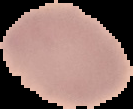
Summary:
  - Image type: segmented cell region on a black background
  - Preparation: thin blood film
  - Result: no malaria parasites seen
  - Image size: 133×109 pixels